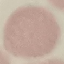
{
  "malaria_status": "uninfected",
  "image_type": "cell patch, automatically extracted from a larger field of view and resized to 64 × 64 pixels",
  "capture": "smartphone camera at the microscope eyepiece",
  "stain": "Giemsa",
  "preparation": "thin blood film"
}